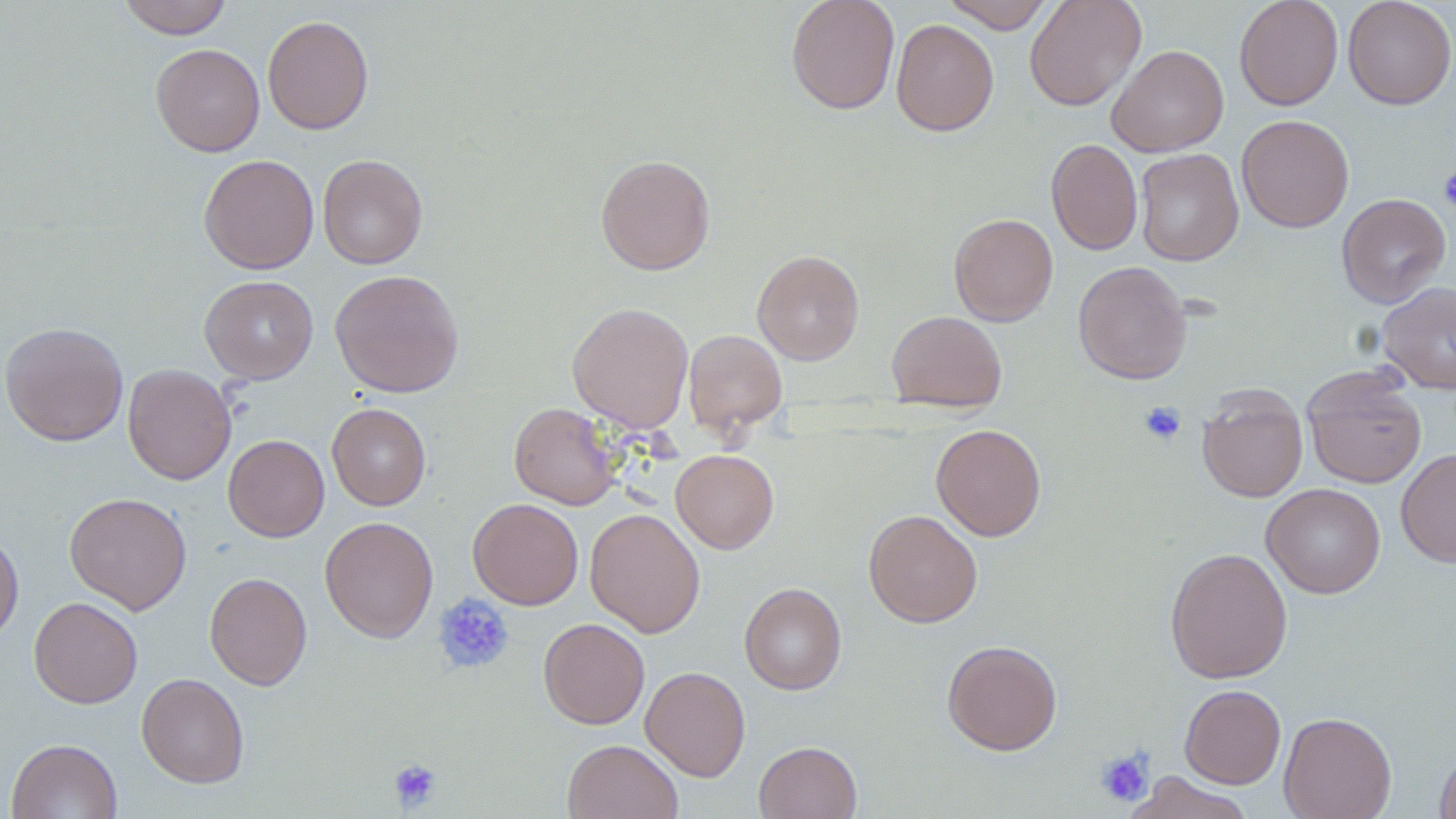
slide-level diagnosis = no evidence of blood parasites
preparation = thin blood smear
image size = 1456×819 pixels
magnification = 1000x
stain = May-Grünwald-Giemsa
uninfected red blood cell locations = approximate bounding boxes as named x1/y1/x2/y2 corners in pixels: (x1=117, y1=0, x2=234, y2=39), (x1=785, y1=0, x2=900, y2=114), (x1=941, y1=0, x2=1055, y2=33), (x1=1024, y1=0, x2=1147, y2=111), (x1=1234, y1=0, x2=1343, y2=110), (x1=1342, y1=0, x2=1456, y2=110), (x1=262, y1=14, x2=374, y2=135), (x1=891, y1=19, x2=998, y2=136), (x1=151, y1=43, x2=265, y2=156), (x1=1106, y1=44, x2=1229, y2=157), (x1=1236, y1=114, x2=1354, y2=233), (x1=1046, y1=138, x2=1143, y2=255), (x1=1134, y1=148, x2=1244, y2=266), (x1=317, y1=153, x2=428, y2=269), (x1=199, y1=154, x2=319, y2=274), (x1=595, y1=154, x2=715, y2=275), (x1=1336, y1=193, x2=1451, y2=308), (x1=948, y1=213, x2=1058, y2=326), (x1=752, y1=250, x2=865, y2=365), (x1=1073, y1=260, x2=1192, y2=385), (x1=330, y1=269, x2=464, y2=398), (x1=199, y1=275, x2=319, y2=383), (x1=1376, y1=281, x2=1456, y2=394), (x1=567, y1=302, x2=694, y2=433), (x1=887, y1=310, x2=1007, y2=412), (x1=1, y1=321, x2=128, y2=446), (x1=683, y1=329, x2=787, y2=434), (x1=122, y1=363, x2=236, y2=485), (x1=1302, y1=368, x2=1427, y2=489), (x1=1197, y1=386, x2=1308, y2=502), (x1=509, y1=402, x2=621, y2=510), (x1=327, y1=403, x2=431, y2=510), (x1=931, y1=423, x2=1047, y2=541), (x1=223, y1=434, x2=329, y2=542), (x1=671, y1=449, x2=779, y2=553), (x1=1396, y1=449, x2=1456, y2=568), (x1=1261, y1=483, x2=1386, y2=599), (x1=64, y1=492, x2=192, y2=615), (x1=468, y1=498, x2=583, y2=609), (x1=585, y1=508, x2=706, y2=638), (x1=863, y1=509, x2=983, y2=628), (x1=319, y1=516, x2=438, y2=642), (x1=0, y1=530, x2=23, y2=647), (x1=1164, y1=547, x2=1293, y2=683), (x1=204, y1=571, x2=312, y2=690), (x1=739, y1=582, x2=847, y2=695), (x1=29, y1=597, x2=143, y2=709), (x1=538, y1=617, x2=650, y2=729), (x1=942, y1=639, x2=1062, y2=755), (x1=640, y1=666, x2=750, y2=781), (x1=136, y1=672, x2=249, y2=788), (x1=1180, y1=684, x2=1286, y2=789), (x1=1278, y1=711, x2=1397, y2=819), (x1=6, y1=738, x2=122, y2=819), (x1=562, y1=739, x2=683, y2=819), (x1=754, y1=741, x2=862, y2=819), (x1=1434, y1=747, x2=1456, y2=819), (x1=1125, y1=771, x2=1255, y2=819)
modality = optical microscopy
field of view = single
platelet locations = approximate bounding boxes as named x1/y1/x2/y2 corners in pixels: (x1=1438, y1=167, x2=1456, y2=214), (x1=1139, y1=401, x2=1187, y2=446), (x1=432, y1=593, x2=515, y2=675), (x1=1095, y1=747, x2=1155, y2=806), (x1=388, y1=758, x2=442, y2=811)